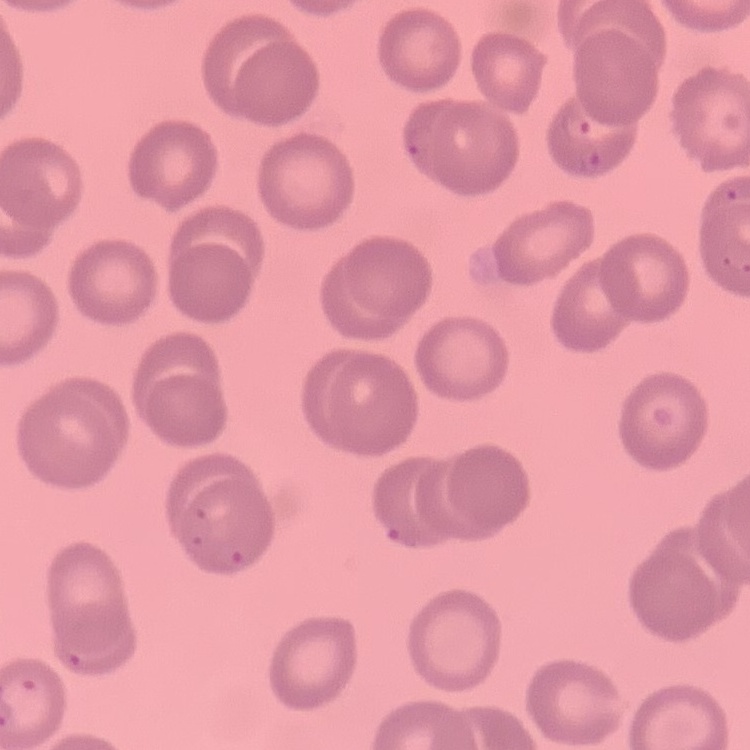

The erythrocytes exhibit no rouleaux formation. Stained with either Field's or Giemsa. One tile cut from a larger photomicrograph. Thin blood smear.